Name the parasite shown.
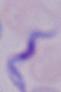

This is a trypanosome.

1000x magnification. Micrograph.